Report the malaria status of this cell.
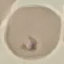

It is parasitized.

Photographed with a smartphone camera at the microscope eyepiece. Cell patch, automatically extracted from a larger field of view and resized to 64 × 64 pixels. Thin smear of blood. Giemsa stain.